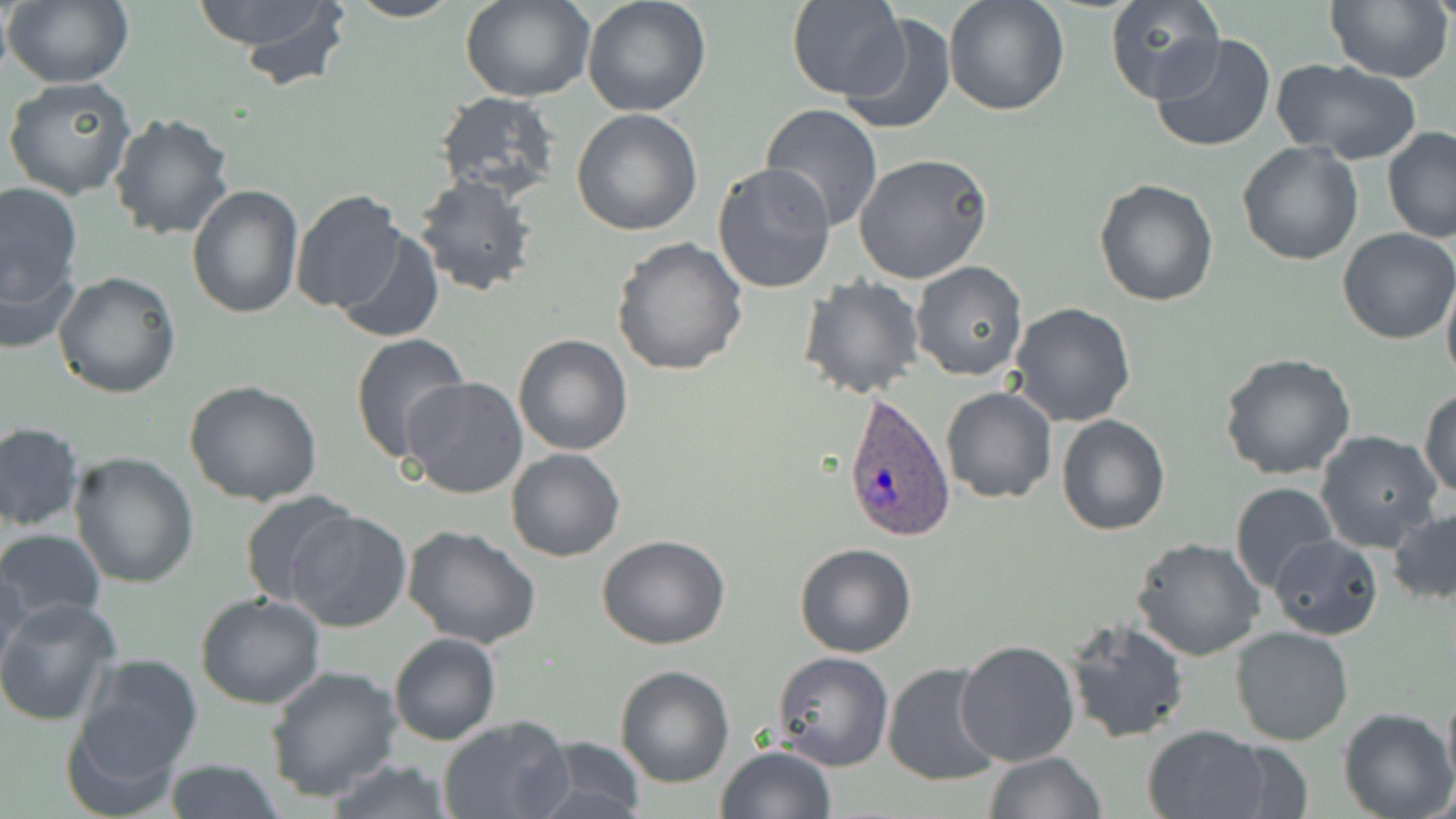
slide-level diagnosis = Plasmodium ovale
image size = 1456×819 pixels
Plasmodium ovale-infected red blood cell locations = approximate bounding boxes as named x1/y1/x2/y2 corners in pixels: (x1=839, y1=392, x2=955, y2=545)
uninfected red blood cell locations = approximate bounding boxes as named x1/y1/x2/y2 corners in pixels: (x1=3, y1=0, x2=132, y2=88), (x1=193, y1=0, x2=349, y2=76), (x1=343, y1=0, x2=462, y2=23), (x1=581, y1=0, x2=712, y2=117), (x1=788, y1=0, x2=906, y2=100), (x1=943, y1=0, x2=1070, y2=117), (x1=1327, y1=0, x2=1456, y2=84), (x1=462, y1=1, x2=595, y2=103), (x1=1103, y1=1, x2=1225, y2=106), (x1=840, y1=12, x2=957, y2=136), (x1=1151, y1=33, x2=1278, y2=154), (x1=1271, y1=58, x2=1422, y2=165), (x1=3, y1=76, x2=135, y2=201), (x1=434, y1=92, x2=563, y2=204), (x1=760, y1=103, x2=883, y2=231), (x1=571, y1=109, x2=703, y2=236), (x1=108, y1=112, x2=236, y2=242), (x1=1382, y1=127, x2=1456, y2=243), (x1=1237, y1=142, x2=1364, y2=265), (x1=854, y1=154, x2=993, y2=286), (x1=712, y1=163, x2=836, y2=295), (x1=412, y1=174, x2=540, y2=297), (x1=1094, y1=177, x2=1220, y2=305), (x1=0, y1=180, x2=83, y2=321), (x1=186, y1=185, x2=305, y2=319), (x1=290, y1=189, x2=408, y2=314), (x1=335, y1=227, x2=445, y2=344), (x1=1337, y1=230, x2=1456, y2=345), (x1=612, y1=237, x2=750, y2=377), (x1=0, y1=251, x2=80, y2=357), (x1=911, y1=261, x2=1028, y2=382), (x1=52, y1=270, x2=181, y2=398), (x1=1441, y1=273, x2=1456, y2=394), (x1=798, y1=275, x2=925, y2=399), (x1=1009, y1=303, x2=1137, y2=427), (x1=348, y1=332, x2=468, y2=464), (x1=513, y1=335, x2=634, y2=456), (x1=1217, y1=351, x2=1357, y2=480), (x1=401, y1=377, x2=528, y2=500), (x1=183, y1=379, x2=323, y2=506), (x1=942, y1=387, x2=1056, y2=505), (x1=1419, y1=387, x2=1456, y2=499), (x1=1056, y1=413, x2=1171, y2=535), (x1=0, y1=422, x2=85, y2=532), (x1=1315, y1=431, x2=1444, y2=554), (x1=506, y1=448, x2=627, y2=562), (x1=68, y1=452, x2=199, y2=590), (x1=1229, y1=483, x2=1338, y2=595), (x1=238, y1=489, x2=360, y2=607), (x1=1388, y1=507, x2=1456, y2=607), (x1=285, y1=508, x2=412, y2=633), (x1=0, y1=526, x2=106, y2=630), (x1=401, y1=526, x2=542, y2=649), (x1=596, y1=534, x2=731, y2=651), (x1=1267, y1=534, x2=1383, y2=640), (x1=1130, y1=538, x2=1264, y2=662), (x1=794, y1=543, x2=919, y2=658), (x1=0, y1=565, x2=32, y2=678), (x1=194, y1=594, x2=326, y2=710), (x1=0, y1=598, x2=121, y2=726), (x1=1063, y1=616, x2=1190, y2=744), (x1=1230, y1=627, x2=1356, y2=746), (x1=388, y1=632, x2=500, y2=745), (x1=953, y1=639, x2=1081, y2=766), (x1=772, y1=651, x2=893, y2=772), (x1=67, y1=654, x2=203, y2=803), (x1=882, y1=662, x2=1005, y2=786), (x1=264, y1=665, x2=404, y2=801), (x1=615, y1=665, x2=736, y2=787), (x1=1441, y1=683, x2=1456, y2=795), (x1=1338, y1=707, x2=1454, y2=819), (x1=436, y1=715, x2=573, y2=819), (x1=1142, y1=724, x2=1274, y2=819), (x1=524, y1=735, x2=650, y2=818), (x1=715, y1=745, x2=836, y2=819), (x1=984, y1=751, x2=1105, y2=819), (x1=321, y1=758, x2=458, y2=817), (x1=165, y1=759, x2=284, y2=818)
modality = optical microscopy
stain = May-Grünwald-Giemsa
preparation = thin blood film
field of view = single
magnification = 1000x